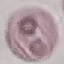
{
  "result": "no malaria parasites detected",
  "image_type": "cell patch, automatically extracted from a larger field of view and resized to 64 × 64 pixels",
  "stain": "Giemsa",
  "preparation": "thin smear",
  "capture": "smartphone through the microscope eyepiece"
}